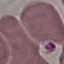
Result: no malaria parasites seen. Giemsa stain. Photographed with a smartphone camera at the microscope eyepiece. Automatically extracted cell patch, resized to 64 × 64 pixels. Thin smear of blood.